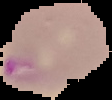 Segmented cell region on a black background. Image is 112×100 pixels. From a thin blood film. Malaria status: parasitized.